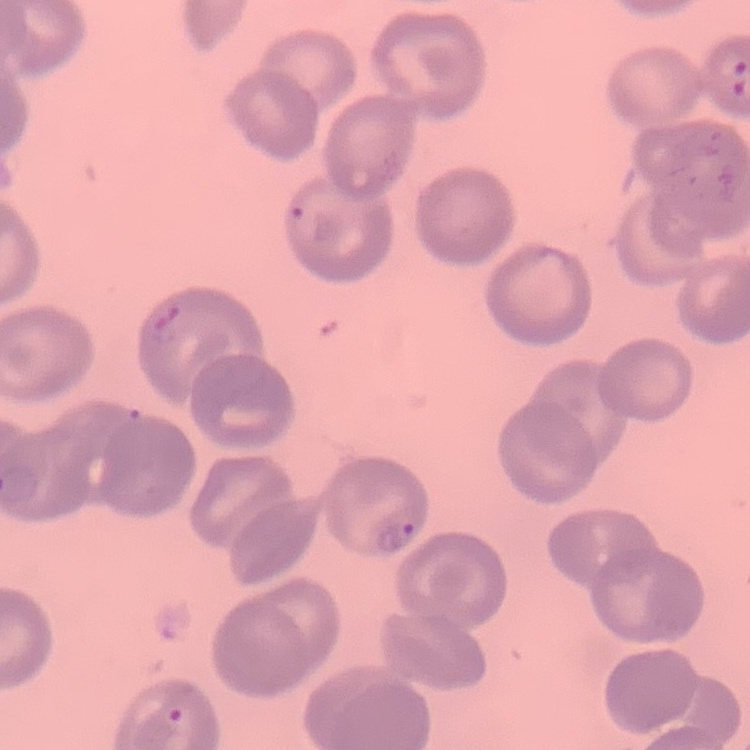

Summary:
  - Erythrocyte morphology: no rouleaux formation
  - Stain: Field's or Giemsa
  - Image type: square crop of a larger photomicrograph
  - Preparation: thin blood smear